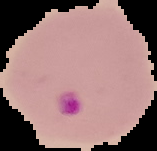

Summary:
  - Image size: 157×151 pixels
  - Malaria status: parasitized
  - Image type: segmented cell region with the area outside set to black
  - Preparation: thin blood film